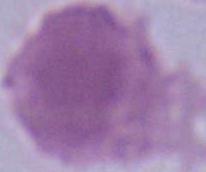
modality: photomicrograph
magnification: 1000x
identification: erythrocyte